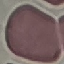

Result: no malaria parasites detected. Cell patch, automatically extracted from a larger field of view and resized to 64 × 64 pixels. Thin blood smear. Giemsa stain. Acquired by smartphone through the microscope eyepiece.